Classify this cell by malaria status.
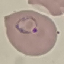

It is parasitized.

Giemsa-stained preparation. Thin smear of blood. Automatically extracted cell patch, resized to 64 × 64 pixels. Photographed with a smartphone camera at the microscope eyepiece.